Locate every Plasmodium parasite.
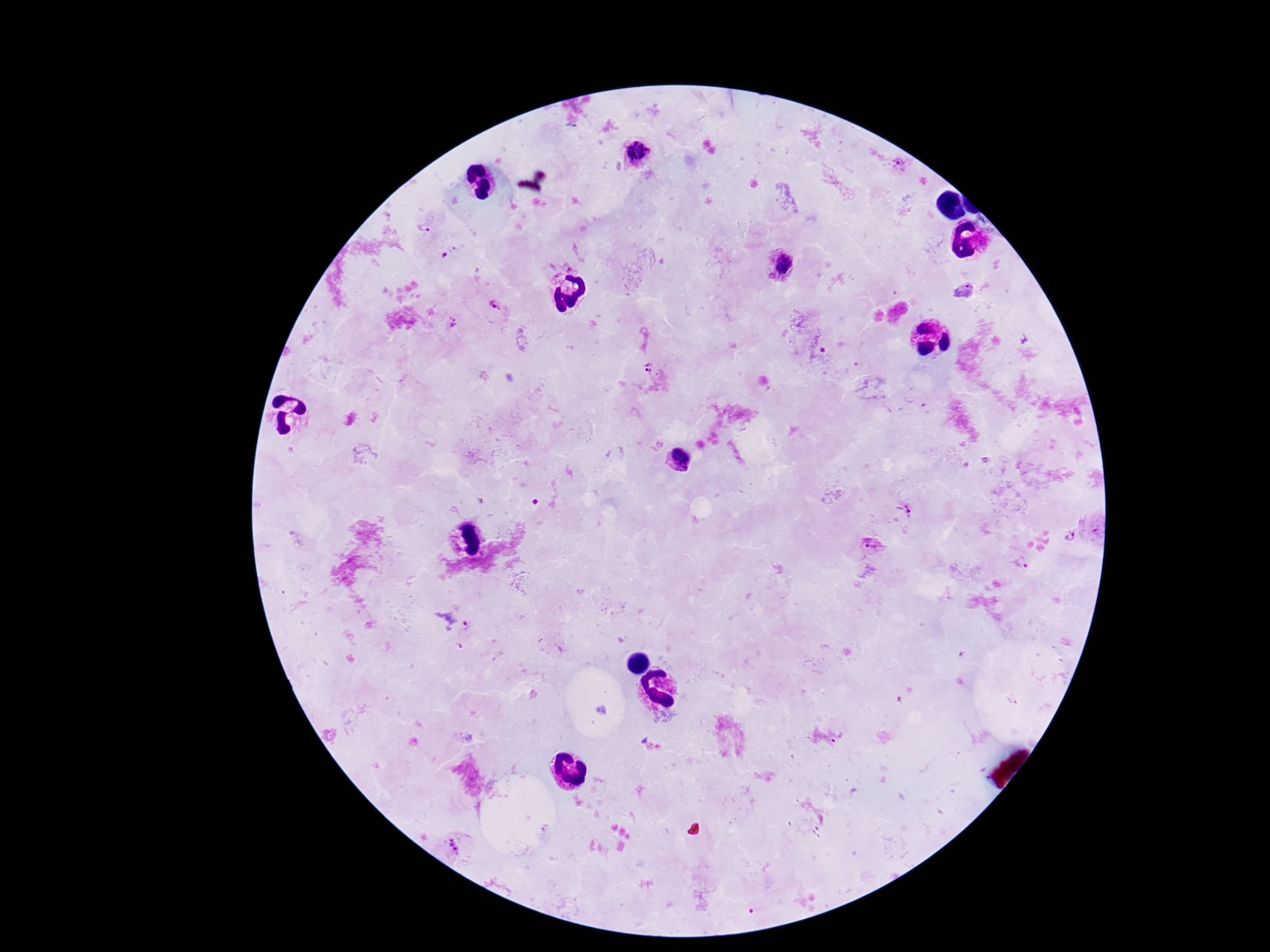

Approximate centers as {x, y} in pixels.
Plasmodium parasites: {636, 155}, {897, 163}, {425, 228}, {782, 264}, {963, 292}, {497, 306}, {452, 324}, {650, 367}, {676, 459}, {907, 511}, {1070, 537}, {873, 544}, {1024, 562}, {458, 846}.

image size = 1270×952 pixels
field of view = one from this slide
magnification = 100x
preparation = thick blood film
capture = smartphone camera through the microscope eyepiece
stain = Giemsa
patient malaria status = positive